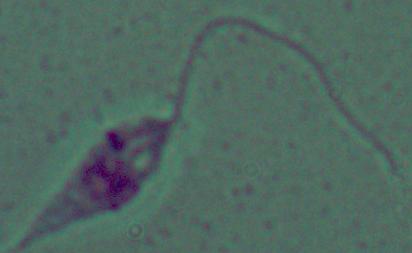
modality = micrograph
identification = Leishmania
magnification = 1000x